Identify the parasite.
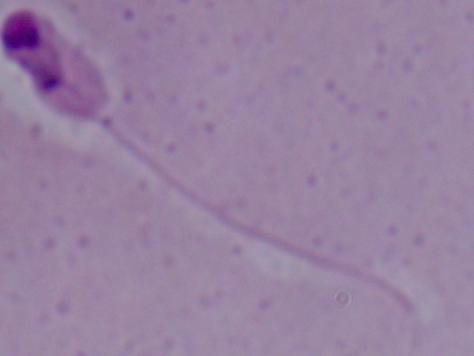
This is Leishmania.

Summary:
  - Modality: photomicrograph
  - Magnification: 1000x